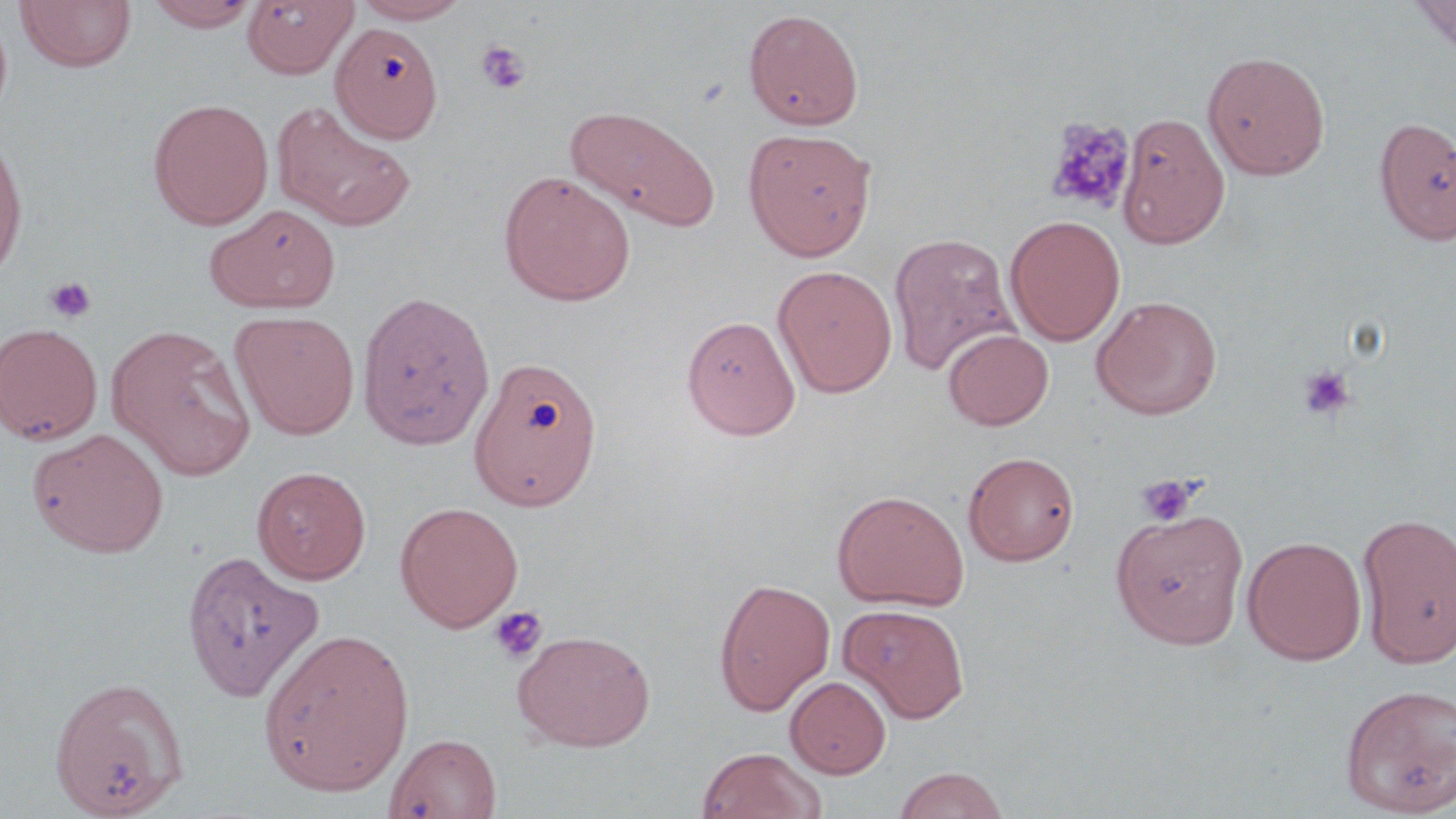
{
  "slide_level_diagnosis": "negative for blood parasites",
  "platelet_locations": "approximate bounding boxes as named x1/y1/x2/y2 corners in pixels: (x1=476, y1=40, x2=531, y2=95), (x1=1044, y1=116, x2=1136, y2=215), (x1=45, y1=276, x2=97, y2=324), (x1=1297, y1=364, x2=1357, y2=422), (x1=1135, y1=473, x2=1201, y2=528), (x1=489, y1=605, x2=548, y2=664)",
  "field_of_view": "single",
  "magnification": "1000x",
  "image_size": "1456×819 pixels",
  "preparation": "thin blood film",
  "stain": "May-Grünwald-Giemsa",
  "modality": "light microscopy",
  "uninfected_red_blood_cell_locations": "approximate bounding boxes as named x1/y1/x2/y2 corners in pixels: (x1=144, y1=0, x2=260, y2=31), (x1=242, y1=0, x2=356, y2=78), (x1=353, y1=0, x2=471, y2=24), (x1=1411, y1=0, x2=1456, y2=54), (x1=14, y1=1, x2=137, y2=73), (x1=743, y1=8, x2=864, y2=130), (x1=331, y1=22, x2=443, y2=142), (x1=1203, y1=50, x2=1330, y2=181), (x1=148, y1=97, x2=274, y2=229), (x1=271, y1=101, x2=416, y2=232), (x1=566, y1=105, x2=721, y2=230), (x1=1117, y1=112, x2=1230, y2=249), (x1=1373, y1=115, x2=1456, y2=246), (x1=743, y1=128, x2=876, y2=261), (x1=0, y1=131, x2=29, y2=283), (x1=499, y1=171, x2=636, y2=306), (x1=206, y1=204, x2=341, y2=313), (x1=1005, y1=215, x2=1125, y2=346), (x1=888, y1=232, x2=1018, y2=377), (x1=773, y1=265, x2=897, y2=398), (x1=357, y1=290, x2=496, y2=450), (x1=1091, y1=295, x2=1222, y2=420), (x1=230, y1=310, x2=360, y2=439), (x1=681, y1=315, x2=800, y2=439), (x1=0, y1=323, x2=103, y2=445), (x1=108, y1=324, x2=256, y2=478), (x1=942, y1=328, x2=1054, y2=430), (x1=468, y1=355, x2=604, y2=511), (x1=27, y1=427, x2=170, y2=557), (x1=963, y1=450, x2=1081, y2=566), (x1=252, y1=465, x2=371, y2=584), (x1=832, y1=489, x2=969, y2=611), (x1=394, y1=501, x2=523, y2=632), (x1=1111, y1=508, x2=1250, y2=648), (x1=1357, y1=511, x2=1456, y2=669), (x1=1242, y1=535, x2=1367, y2=665), (x1=180, y1=551, x2=321, y2=701), (x1=714, y1=578, x2=835, y2=715), (x1=838, y1=604, x2=970, y2=723), (x1=258, y1=628, x2=414, y2=796), (x1=512, y1=629, x2=655, y2=751), (x1=785, y1=675, x2=891, y2=778), (x1=48, y1=676, x2=189, y2=818), (x1=1339, y1=682, x2=1455, y2=815), (x1=385, y1=732, x2=502, y2=818), (x1=696, y1=747, x2=826, y2=819), (x1=892, y1=766, x2=1011, y2=819)"
}